Identify the parasite.
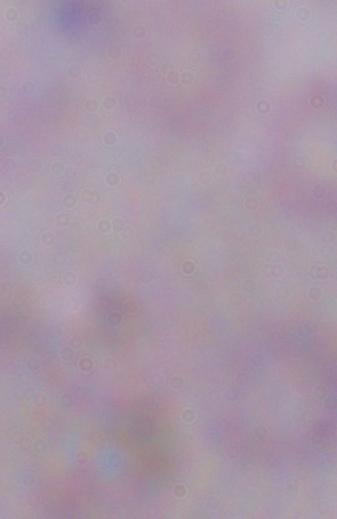

This is a trypanosome.

Photomicrograph. 1000x magnification.